Comment on the morphology of the erythrocytes.
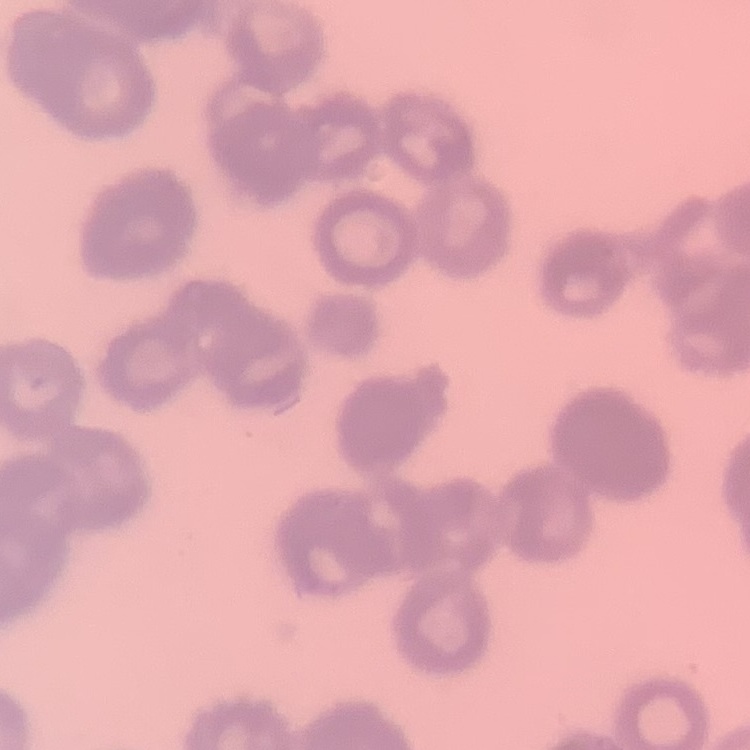
Rouleaux formation.

preparation = thin blood film
stain = Field's or Giemsa
image type = square crop of a larger photomicrograph